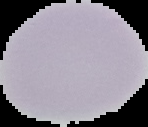
Summary:
  - Image size: 148×127 pixels
  - Image type: cell region segmented out of the field of view; surrounding area masked to black
  - Preparation: thin blood film
  - Result: no malaria parasites detected